Report the malaria status of this cell.
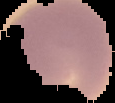

It is uninfected.

image type = segmented cell region with the area outside set to black
image size = 115×103 pixels
preparation = thin blood smear